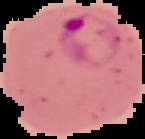 Result: malaria parasites identified. From a thin blood smear. Cell region segmented out of the field of view; the surrounding area is masked to black. Image is 145×139 pixels.